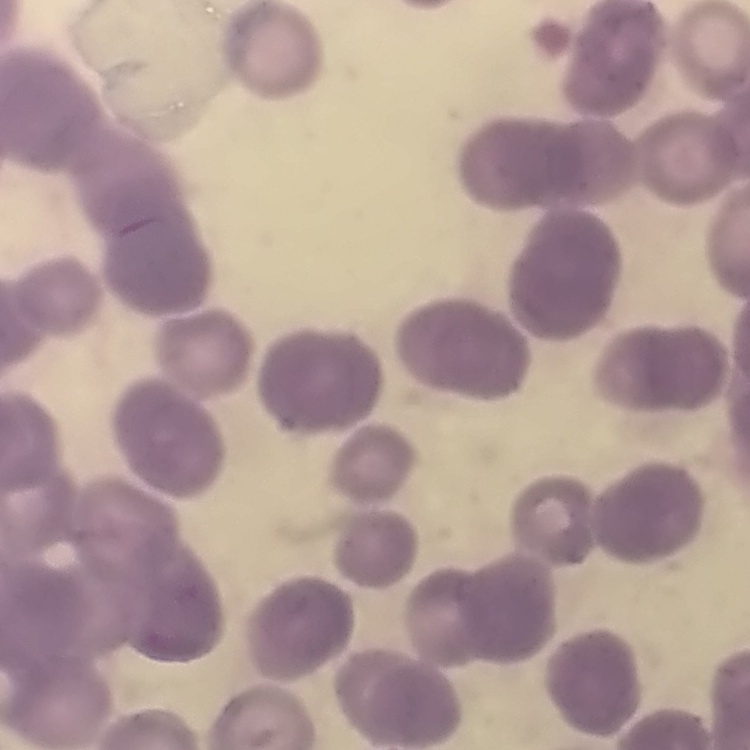

erythrocyte morphology = rouleaux formation
stain = Field's or Giemsa
preparation = thin blood film
image type = one tile cut from a larger photomicrograph